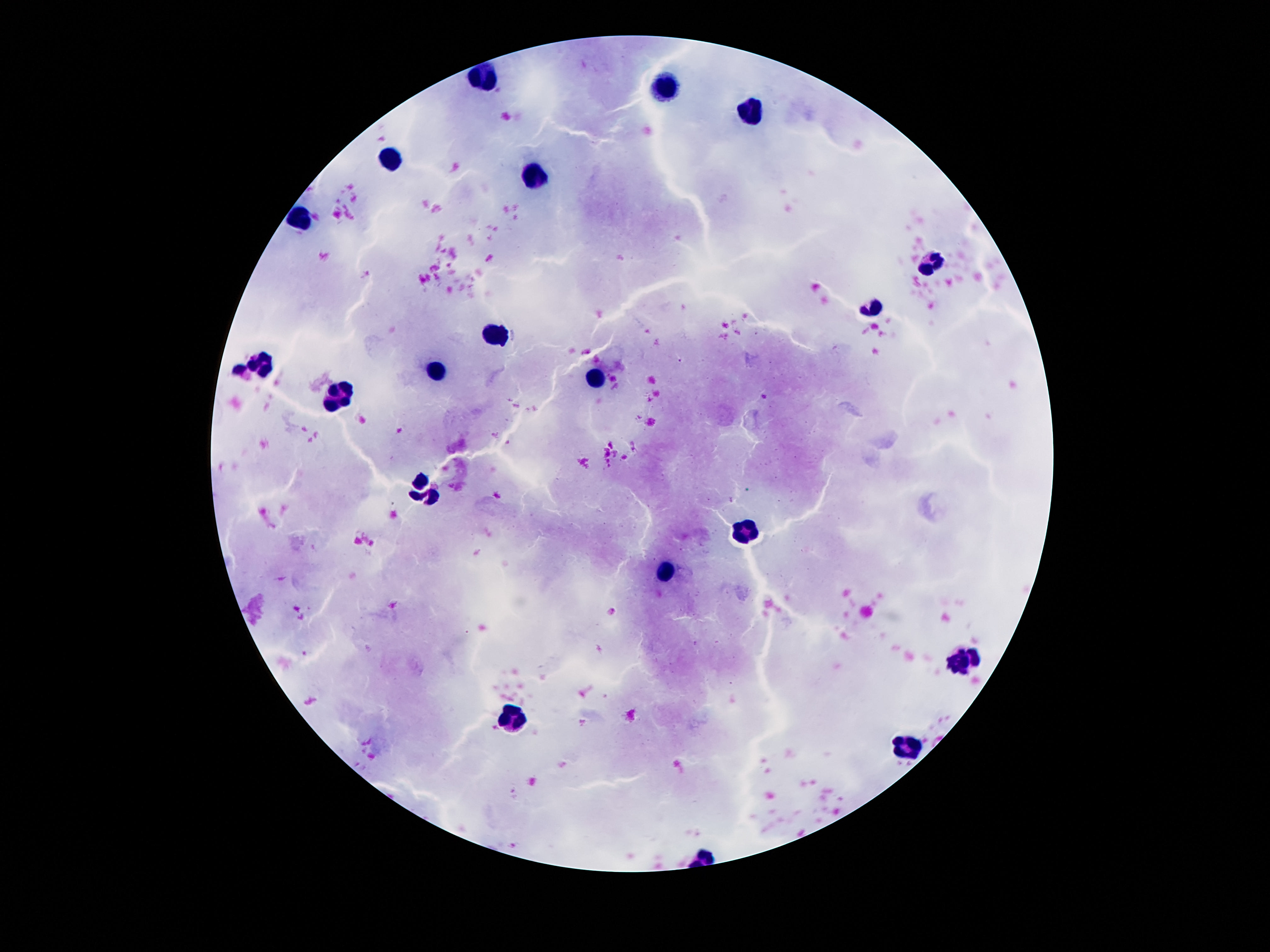
Approximate centers as [x, y] in pixels.
Summary:
  - Leukocyte locations: [483, 75], [664, 85], [752, 107], [387, 160], [534, 172], [298, 222], [932, 261], [874, 308], [498, 336], [262, 365], [439, 369], [597, 376], [342, 397], [428, 489], [746, 529], [668, 569], [960, 659], [512, 720], [911, 744]
  - Patient malaria status: uninfected
  - Image size: 1270×952 pixels
  - Stain: Giemsa
  - Magnification: 100x
  - Capture: smartphone camera through the microscope eyepiece
  - Field of view: one from this slide
  - Preparation: thick blood smear